State which parasite is depicted.
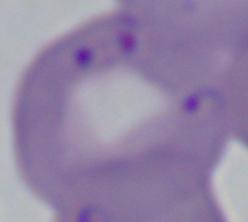
This is Babesia.

magnification = 1000x
modality = micrograph